Assess the morphology of the erythrocytes.
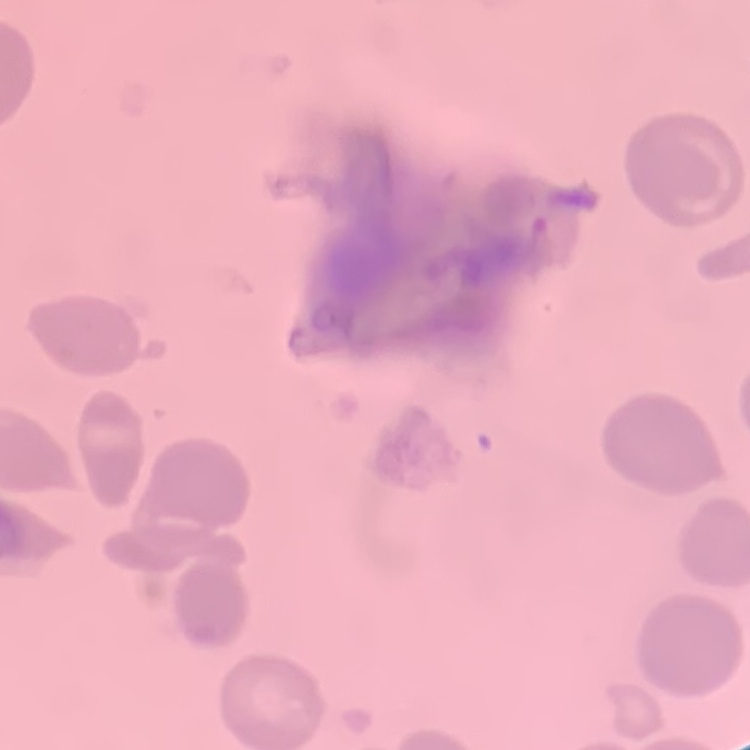
They show no rouleaux formation.

Summary:
  - Image type: square crop of a larger photomicrograph
  - Preparation: thin blood film
  - Stain: Field's or Giemsa